Outline each blood parasite and name the species.
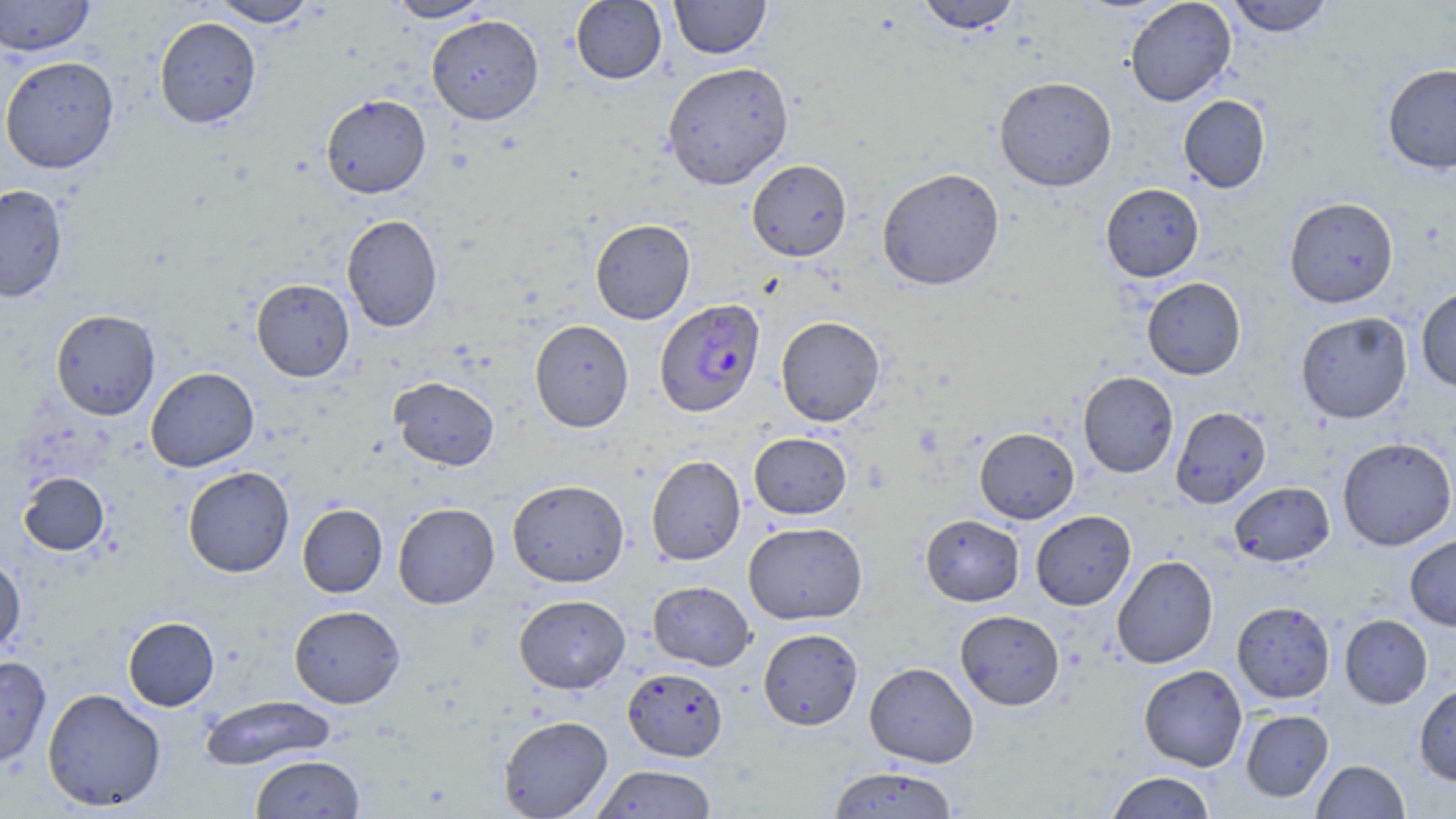

Approximate bounding boxes as (x1, y1, x2, y2) in pixels.
Plasmodium falciparum-infected red blood cells: (654, 298, 765, 417).
No Plasmodium ovale, Plasmodium malariae, Plasmodium vivax, Babesia divergens, or Trypanosoma brucei observed.

slide-level diagnosis = Plasmodium falciparum
preparation = thin blood film
uninfected red blood cell locations = approximate bounding boxes as (x1, y1, x2, y2) in pixels: (0, 0, 95, 57), (207, 0, 318, 28), (387, 0, 495, 22), (570, 0, 667, 85), (669, 0, 772, 59), (914, 0, 1023, 35), (1125, 0, 1237, 107), (1226, 0, 1334, 37), (426, 14, 544, 125), (154, 17, 262, 129), (0, 56, 119, 174), (662, 61, 794, 190), (1381, 62, 1456, 174), (993, 75, 1117, 192), (320, 94, 432, 198), (1178, 95, 1271, 193), (747, 159, 852, 261), (876, 167, 1005, 291), (1101, 183, 1204, 282), (0, 184, 68, 302), (1284, 196, 1399, 308), (341, 214, 443, 332), (590, 218, 695, 324), (1142, 277, 1246, 380), (251, 278, 354, 382), (1416, 286, 1456, 392), (50, 309, 160, 420), (1295, 311, 1412, 424), (776, 315, 885, 426), (530, 320, 634, 432), (145, 367, 259, 472), (1078, 371, 1178, 477), (389, 376, 499, 470), (1170, 406, 1271, 509), (974, 427, 1079, 524), (749, 432, 852, 520), (1337, 437, 1456, 551), (646, 454, 745, 565), (182, 466, 295, 578), (18, 472, 110, 556), (507, 479, 629, 587), (1229, 481, 1334, 567), (393, 502, 500, 609), (297, 503, 387, 598), (1031, 510, 1136, 610), (921, 514, 1024, 606), (743, 521, 868, 624), (1405, 534, 1456, 631), (0, 554, 26, 655), (1112, 555, 1218, 668), (647, 581, 755, 670), (513, 594, 630, 694), (1231, 601, 1335, 703), (288, 605, 406, 708), (955, 610, 1064, 710), (1339, 614, 1432, 709), (123, 616, 220, 711), (757, 628, 863, 730), (0, 655, 51, 768), (864, 662, 979, 768), (1139, 664, 1248, 771), (623, 667, 728, 761), (1414, 684, 1456, 786), (42, 688, 166, 811), (200, 695, 337, 771), (1241, 709, 1333, 802), (498, 715, 613, 818), (249, 753, 365, 818), (1311, 759, 1410, 818), (591, 764, 718, 818), (827, 766, 959, 818), (1105, 771, 1217, 818)
field of view = single
magnification = 1000x
image size = 1456×819 pixels
stain = May-Grünwald-Giemsa
modality = optical microscopy